Identify the blood parasite species.
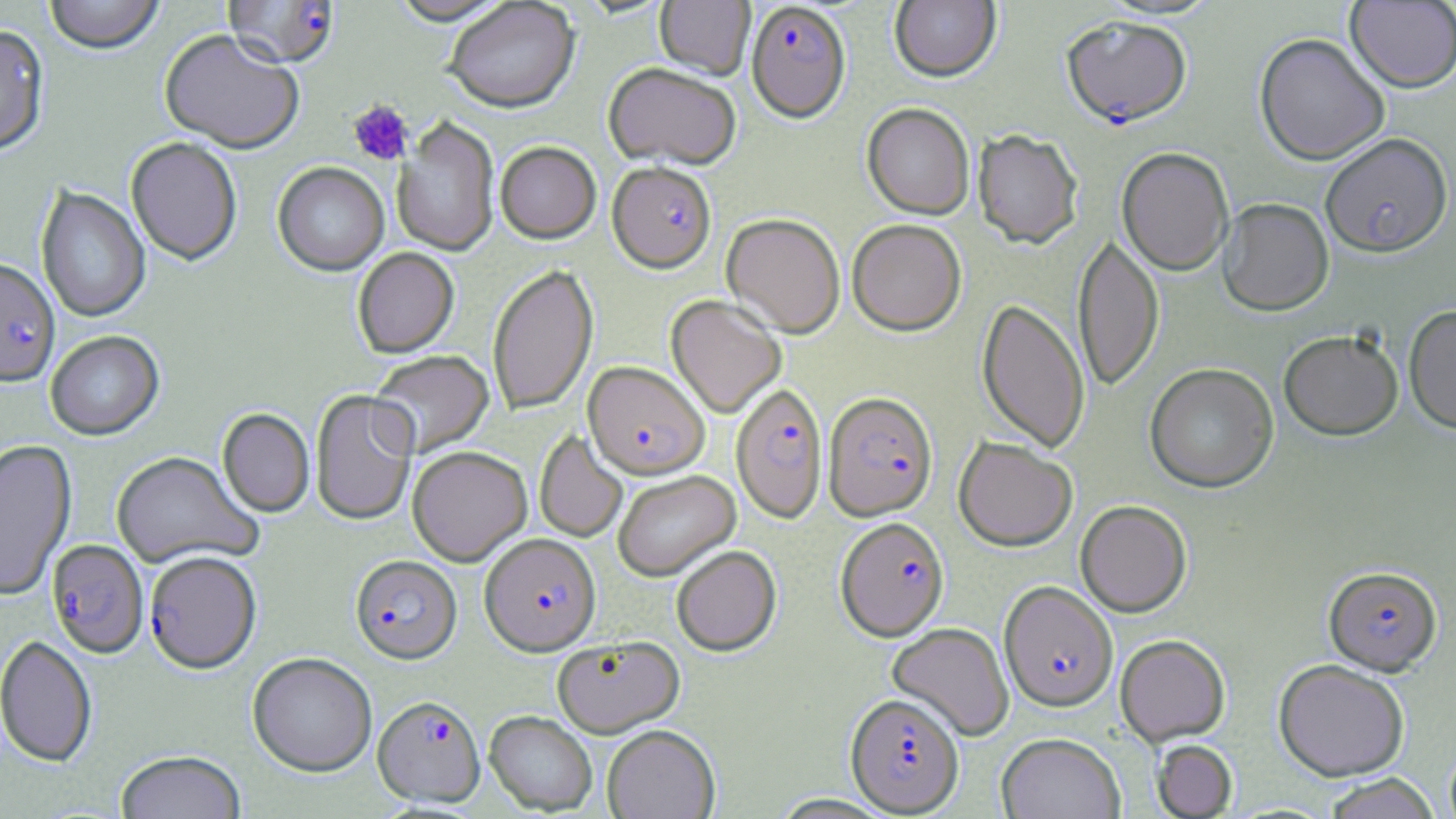

Plasmodium falciparum.

Approximate bounding boxes as (x1, y1, x2, y2) in pixels. Platelet locations: (347, 100, 413, 167). Plasmodium falciparum-infected red blood cell locations: (221, 1, 340, 72), (746, 3, 852, 127), (1061, 18, 1192, 131), (607, 165, 716, 276), (0, 261, 60, 390), (582, 363, 710, 481), (731, 385, 827, 525), (822, 393, 938, 523), (835, 518, 949, 642), (479, 536, 602, 659), (46, 540, 149, 660), (144, 553, 261, 677), (350, 557, 462, 667), (1324, 566, 1442, 675), (999, 582, 1117, 711), (845, 694, 964, 816), (372, 698, 486, 810). Uninfected red blood cell locations: (44, 0, 164, 57), (388, 0, 512, 28), (655, 0, 755, 82), (889, 0, 1001, 85), (1095, 0, 1222, 21), (1346, 1, 1456, 93), (444, 2, 580, 117), (0, 26, 50, 159), (158, 32, 303, 157), (1254, 33, 1391, 166), (603, 66, 740, 172), (862, 105, 974, 221), (392, 118, 499, 259), (972, 131, 1083, 252), (1320, 135, 1453, 260), (126, 139, 242, 267), (495, 143, 601, 245), (1117, 149, 1233, 277), (272, 163, 389, 277), (36, 187, 151, 325), (1218, 200, 1334, 318), (721, 215, 845, 341), (847, 222, 966, 337), (1073, 234, 1164, 393), (352, 248, 460, 359), (487, 264, 599, 416), (665, 296, 785, 419), (976, 299, 1090, 455), (1403, 305, 1456, 437), (1279, 330, 1403, 442), (45, 332, 165, 443), (369, 350, 495, 458), (1145, 363, 1279, 494), (309, 391, 418, 527), (217, 409, 314, 519), (534, 430, 628, 544), (954, 437, 1077, 550), (0, 441, 77, 601), (408, 449, 532, 567), (111, 452, 262, 570), (614, 472, 741, 583), (1075, 500, 1192, 617), (671, 548, 782, 658), (887, 623, 1014, 741), (1115, 634, 1230, 746), (0, 637, 97, 769), (552, 638, 685, 740), (247, 654, 377, 779), (1273, 659, 1410, 781), (483, 713, 597, 816), (602, 727, 720, 819), (996, 732, 1126, 819), (1152, 739, 1238, 818), (1445, 743, 1456, 819), (115, 752, 246, 819), (1320, 773, 1441, 819). Single field of view. 1000x magnification. Thin blood film. Light microscopy. Image is 1456×819 pixels. May-Grünwald-Giemsa-stained preparation.